Outline each blood parasite and name the species.
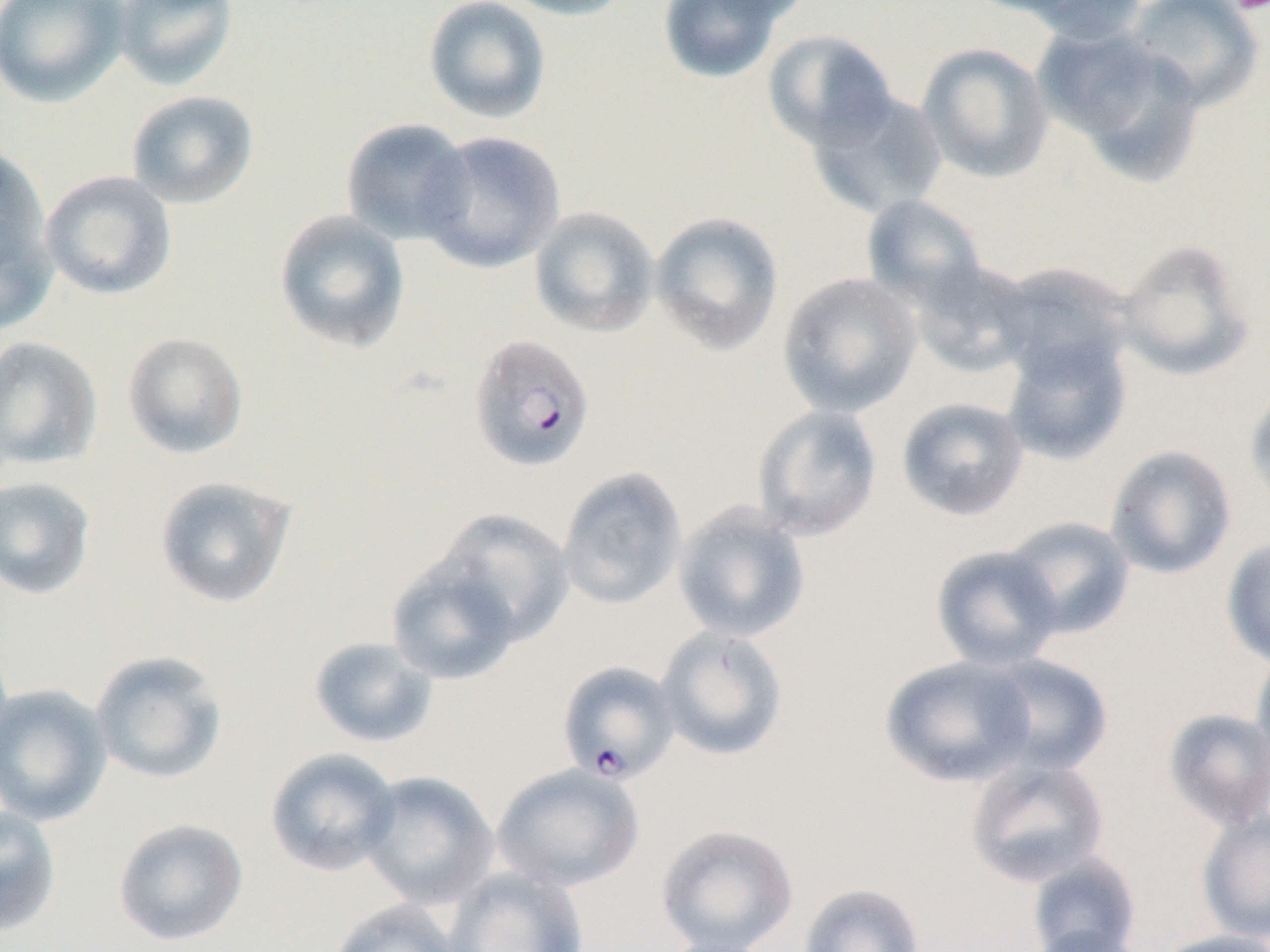

Approximate bounding boxes as (x1, y1, x2, y2) in pixels.
Plasmodium falciparum-infected red blood cells (subset): (468, 333, 595, 471).
No Plasmodium ovale, Plasmodium malariae, Plasmodium vivax, Babesia divergens, or Trypanosoma brucei observed.

Summary:
  - Uninfected red blood cell locations (subset): (0, 0, 128, 107), (110, 0, 239, 92), (423, 0, 552, 125), (499, 0, 635, 21), (657, 0, 791, 84), (991, 0, 1150, 42), (1122, 0, 1263, 111), (1038, 27, 1206, 185), (762, 29, 898, 150), (917, 43, 1054, 184), (806, 87, 948, 219), (126, 90, 259, 209), (341, 118, 475, 246), (417, 131, 566, 273), (0, 141, 51, 284), (40, 171, 177, 301), (862, 195, 991, 310), (0, 206, 57, 338), (529, 207, 661, 338), (274, 210, 410, 353), (650, 212, 784, 355), (1113, 238, 1257, 383), (905, 255, 1038, 377), (992, 261, 1137, 384), (778, 272, 922, 418), (122, 331, 249, 459), (1000, 335, 1132, 466), (0, 336, 102, 471), (1245, 385, 1270, 513), (896, 397, 1029, 522), (752, 404, 883, 543), (1105, 444, 1237, 579), (557, 466, 688, 610), (0, 476, 97, 600), (154, 476, 295, 609), (672, 502, 811, 644), (434, 509, 575, 645), (1001, 516, 1135, 639), (1220, 537, 1270, 669), (929, 545, 1063, 672), (385, 554, 524, 685), (656, 626, 789, 762), (307, 636, 439, 748), (1250, 646, 1270, 779), (90, 651, 228, 785), (979, 653, 1114, 777), (879, 655, 1037, 788), (0, 685, 111, 826), (1162, 708, 1270, 831), (265, 748, 401, 877), (965, 756, 1109, 888), (491, 763, 645, 893), (358, 771, 499, 910), (0, 805, 61, 937), (1197, 808, 1270, 944), (112, 817, 249, 947), (655, 823, 799, 952), (1026, 852, 1143, 952), (444, 866, 590, 952), (798, 883, 926, 952), (328, 899, 464, 952), (1024, 924, 1153, 952), (1150, 930, 1270, 952), (654, 933, 778, 952)
  - Platelet locations: (1229, 0, 1270, 16)
  - Slide-level diagnosis: Plasmodium falciparum
  - Field of view: single
  - Magnification: 1000x
  - Modality: optical microscopy
  - Preparation: thin blood smear
  - Image size: 1270×952 pixels